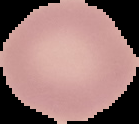
preparation: thin blood film
image_size: 139×124 pixels
image_type: segmented cell region on a black background
malaria_status: uninfected